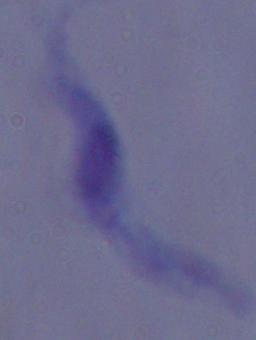

Summary:
  - Modality: micrograph
  - Magnification: 1000x
  - Identification: trypanosome